Classify this cell by malaria status.
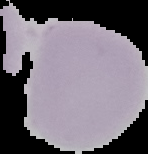

Uninfected.

Summary:
  - Image type: cell region segmented out of the field of view; surrounding area masked to black
  - Image size: 148×154 pixels
  - Preparation: thin blood smear